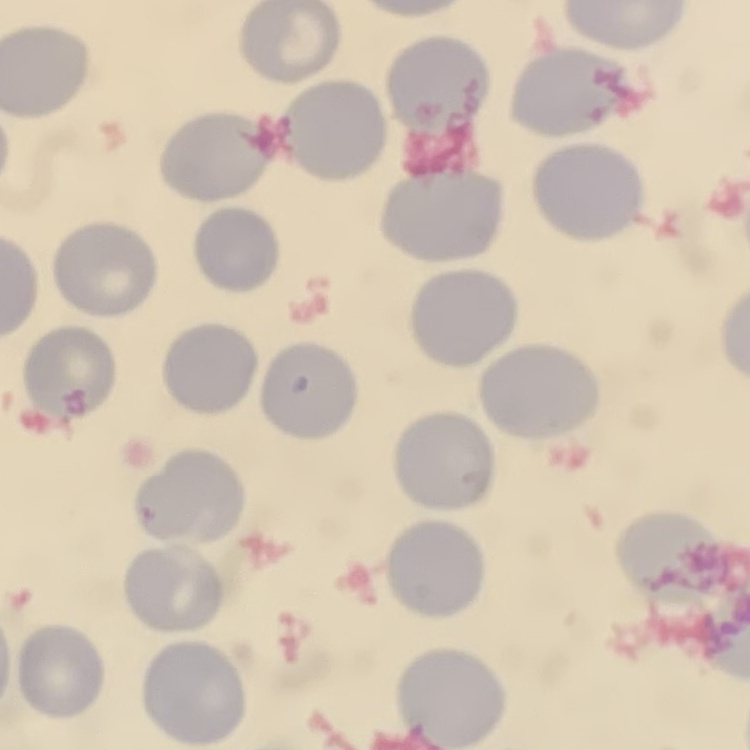 The erythrocytes show no rouleaux formation. Thin peripheral smear. One tile cut from a larger photomicrograph. Field's or Giemsa stain.